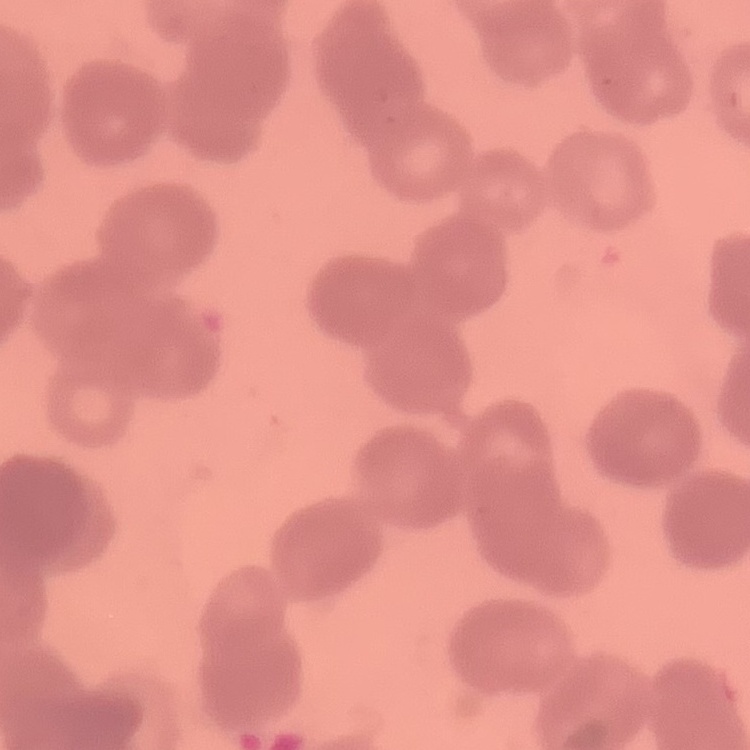
erythrocyte morphology = rouleaux formation
preparation = thin blood smear
stain = Field's or Giemsa
image type = square crop of a larger photomicrograph